Name the parasite shown.
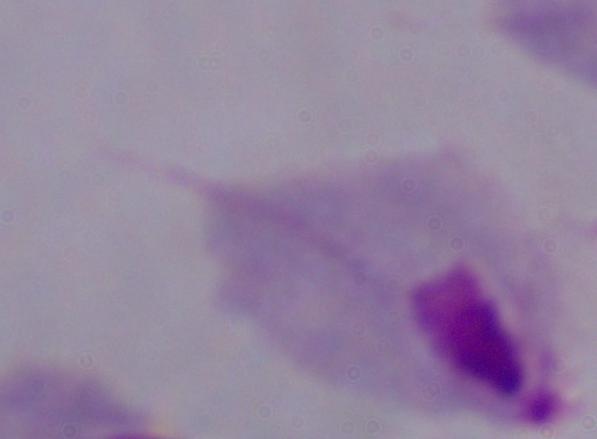
This is a trichomonad.

Summary:
  - Magnification: 1000x
  - Modality: photomicrograph